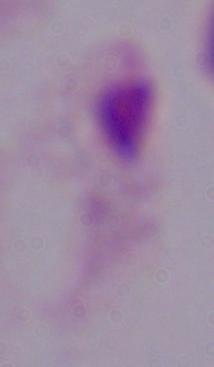

identification: trichomonad
modality: photomicrograph
magnification: 1000x